Report the malaria status of this cell.
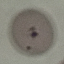
It is uninfected.

Summary:
  - Stain: Giemsa
  - Image type: automatically extracted cell patch, resized to 64 × 64 pixels
  - Preparation: thin smear
  - Capture: smartphone through the microscope eyepiece